Give the extent of all Plasmodium vivax-infected red blood cells.
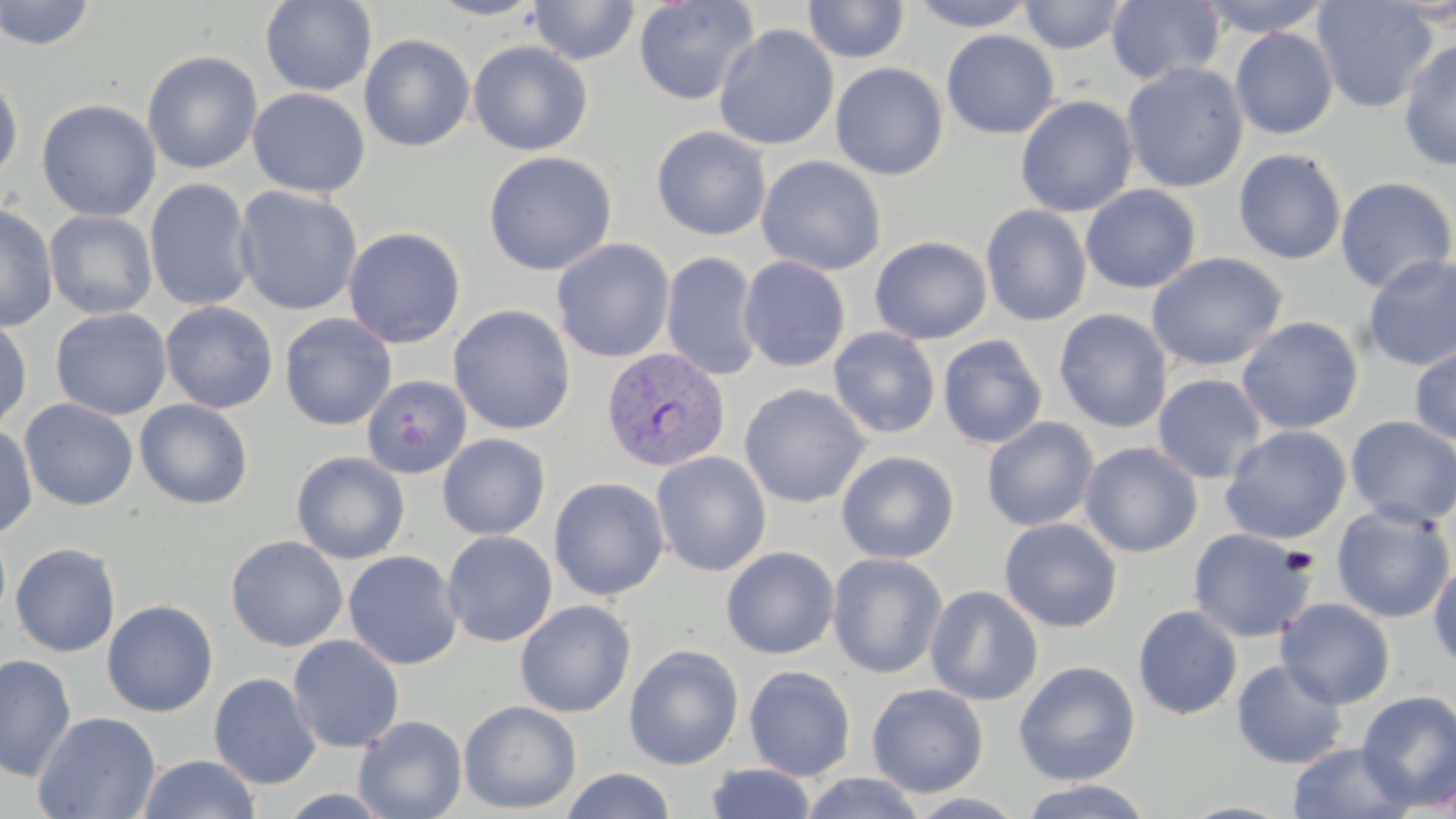
Approximate bounding boxes as (x1,y1)-(x2,y2) corner pairs in pixels.
Plasmodium vivax-infected red blood cells: (601,346)-(731,472).

Uninfected red blood cell locations: (1,0)-(96,51), (260,0)-(377,96), (426,0)-(546,20), (634,0)-(759,106), (803,0)-(910,64), (912,0)-(1035,31), (1019,0)-(1129,54), (1196,0)-(1334,37), (1311,0)-(1437,113), (527,1)-(641,65), (1106,1)-(1225,85), (714,24)-(839,151), (1230,27)-(1339,139), (940,30)-(1059,139), (358,34)-(475,153), (1398,38)-(1456,171), (468,40)-(593,156), (141,50)-(264,174), (1121,61)-(1249,193), (830,62)-(948,180), (0,74)-(24,183), (247,88)-(370,198), (1015,95)-(1138,217), (36,99)-(161,222), (651,126)-(772,241), (1233,148)-(1347,265), (483,151)-(617,276), (756,156)-(886,276), (1334,176)-(1456,294), (144,178)-(256,311), (1080,185)-(1202,294), (233,186)-(363,315), (0,203)-(58,333), (981,204)-(1092,327), (44,210)-(157,320), (343,227)-(466,349), (869,236)-(992,344), (551,239)-(675,363), (661,251)-(763,382), (1146,252)-(1287,371), (1362,254)-(1456,371), (738,256)-(851,372), (160,301)-(279,414), (447,304)-(576,435), (50,307)-(173,420), (1053,309)-(1173,433), (280,313)-(396,431), (1236,316)-(1363,435), (0,317)-(32,433), (828,327)-(941,439), (937,334)-(1048,449), (1409,343)-(1456,446), (1152,374)-(1267,484), (361,376)-(472,479), (739,383)-(869,508), (19,398)-(138,511), (134,399)-(254,510), (1344,416)-(1456,528), (981,417)-(1099,532), (0,423)-(38,539), (1219,425)-(1352,545), (437,433)-(551,541), (1080,442)-(1202,558), (291,451)-(410,564), (651,451)-(772,577), (836,451)-(959,564), (549,477)-(670,601), (1330,504)-(1455,624), (998,518)-(1122,633), (1187,528)-(1316,643), (441,531)-(557,647), (226,535)-(348,651), (10,542)-(121,657), (732,546)-(848,780), (721,547)-(840,659), (343,550)-(463,670), (827,552)-(948,678), (1428,560)-(1456,670), (925,585)-(1043,706), (1276,598)-(1395,709), (515,599)-(636,717), (101,600)-(218,717), (1132,605)-(1243,720), (287,635)-(404,753), (624,644)-(744,770), (0,652)-(77,782), (1013,660)-(1140,785), (1231,660)-(1348,769), (743,666)-(856,781), (209,673)-(321,790), (867,683)-(989,797), (1356,690)-(1456,808), (458,700)-(582,814), (33,711)-(161,819), (353,715)-(467,819), (1287,741)-(1414,819), (137,754)-(261,818), (706,763)-(817,819), (562,767)-(676,819), (800,772)-(926,818), (1018,780)-(1155,819), (906,792)-(1029,819). Slide-level diagnosis: Plasmodium vivax. Thin blood smear. Image is 1456×819 pixels. Single field of view. May-Grünwald-Giemsa stain. Optical microscopy. Captured at 1000x magnification.